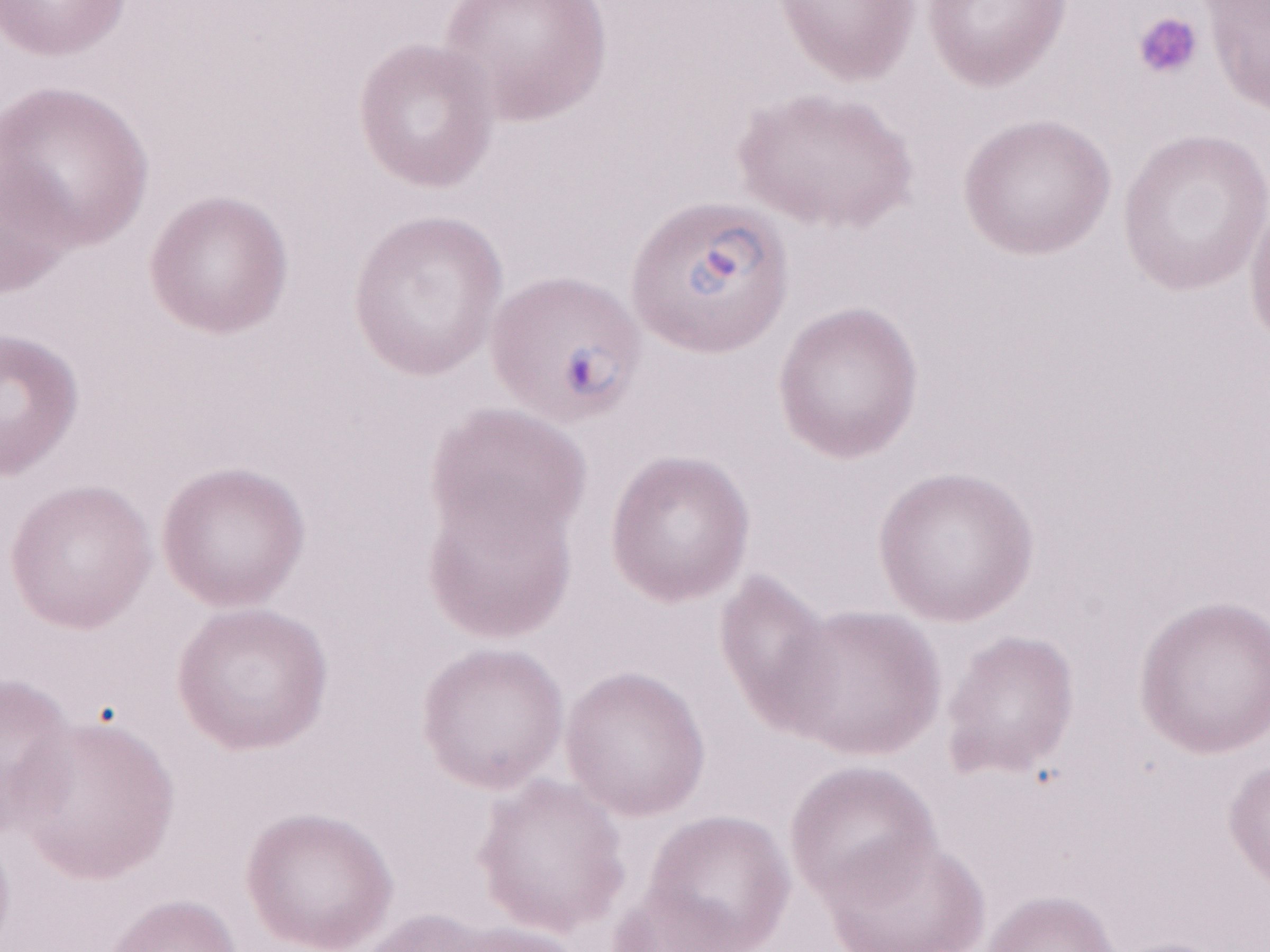 Olympus BX43 microscope and DP73 digital camera. Thin blood film. Image is 1270×952 pixels. Patient diagnosis: malaria infection. One field of this slide. May-Grünwald-Giemsa (MGG) stain. Magnification: 1,000x.